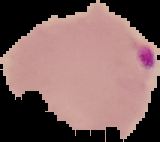

Summary:
  - Image type: segmented cell region with the area outside set to black
  - Image size: 160×142 pixels
  - Preparation: thin blood film
  - Result: Plasmodium parasites identified